State the blood parasite species.
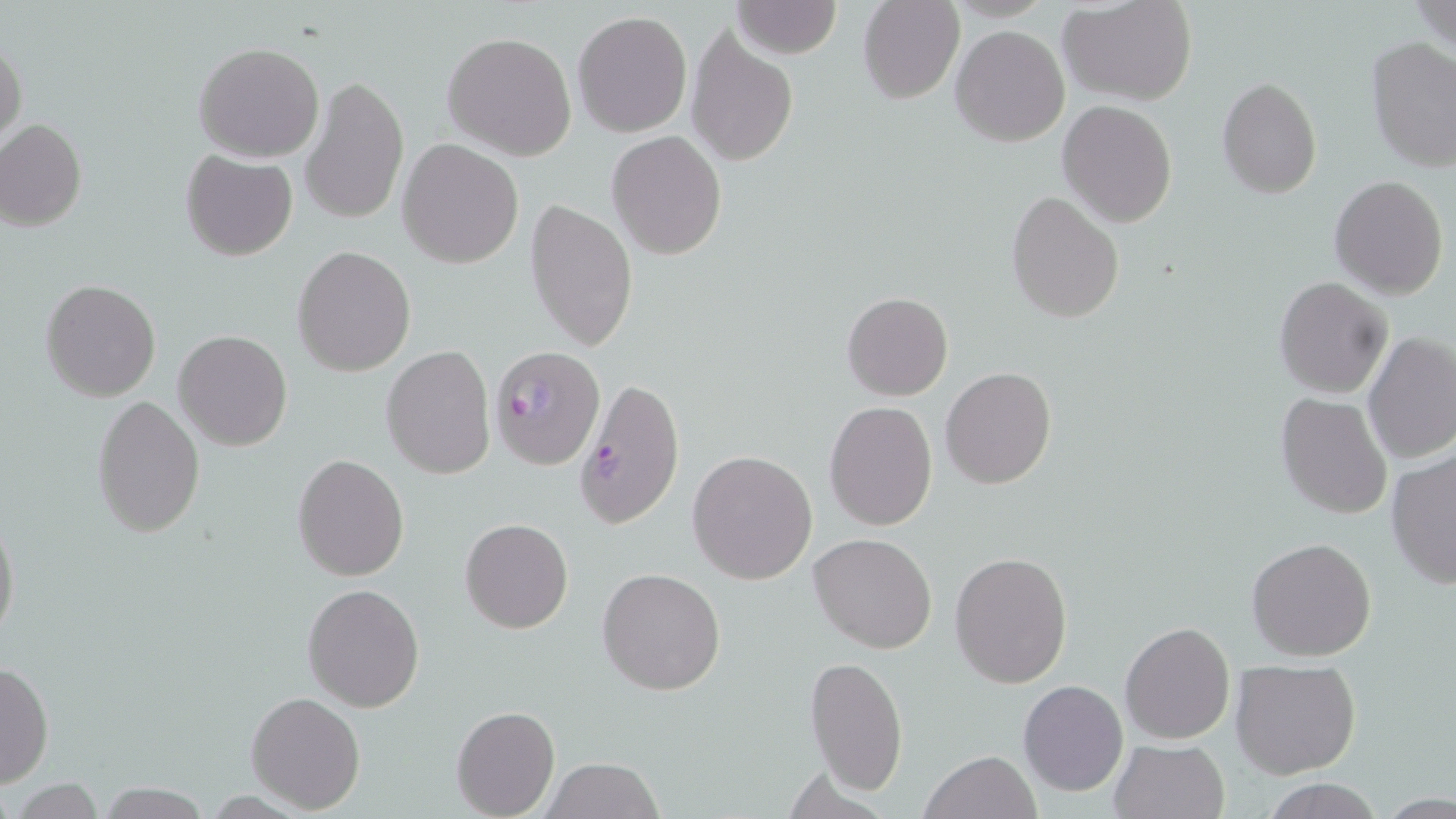

Plasmodium falciparum.

field of view = single
magnification = 1000x
image size = 1456×819 pixels
modality = light microscopy
uninfected red blood cell locations = approximate bounding boxes as [x1, y1, x2, y2] in pixels: [730, 0, 842, 57], [859, 0, 965, 104], [1057, 0, 1200, 106], [1413, 0, 1456, 57], [573, 10, 692, 138], [952, 26, 1071, 147], [684, 27, 799, 167], [442, 32, 577, 160], [1365, 37, 1456, 172], [0, 39, 26, 152], [193, 41, 325, 162], [300, 75, 409, 226], [1216, 77, 1321, 200], [1058, 100, 1177, 225], [0, 120, 86, 231], [607, 130, 726, 259], [398, 140, 524, 267], [180, 150, 297, 261], [1328, 174, 1449, 299], [1005, 190, 1125, 322], [524, 197, 639, 352], [292, 247, 415, 375], [1273, 276, 1393, 398], [42, 280, 162, 402], [841, 291, 952, 402], [173, 330, 293, 451], [1362, 331, 1456, 465], [381, 346, 496, 479], [940, 366, 1057, 490], [1275, 393, 1392, 518], [92, 394, 206, 538], [824, 401, 938, 532], [1386, 449, 1455, 591], [687, 450, 818, 585], [292, 454, 408, 581], [0, 512, 20, 644], [460, 518, 573, 634], [809, 533, 939, 653], [1246, 536, 1378, 662], [950, 551, 1073, 688], [597, 567, 726, 695], [302, 584, 424, 712], [1119, 620, 1235, 744], [803, 655, 909, 799], [1230, 658, 1362, 780], [0, 661, 53, 790], [1018, 679, 1128, 797], [244, 691, 365, 813], [450, 706, 560, 818], [1107, 738, 1232, 819], [918, 750, 1041, 819], [544, 756, 665, 819], [10, 778, 110, 816], [1260, 779, 1385, 817], [93, 783, 214, 817]
stain = May-Grünwald-Giemsa
Plasmodium falciparum-infected red blood cell locations = approximate bounding boxes as [x1, y1, x2, y2] in pixels: [491, 345, 605, 468], [574, 377, 684, 529]
preparation = thin blood smear